Classify this cell by malaria status.
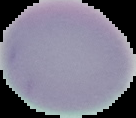

Uninfected.

Image is 136×118 pixels. From a thin blood smear. Cell region segmented out of the field of view; the surrounding area is masked to black.